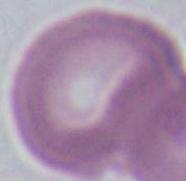 Captured at 1000x magnification. An erythrocyte is seen. Photomicrograph.